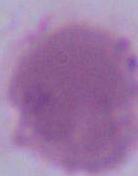

magnification = 1000x
modality = photomicrograph
identification = red blood cell